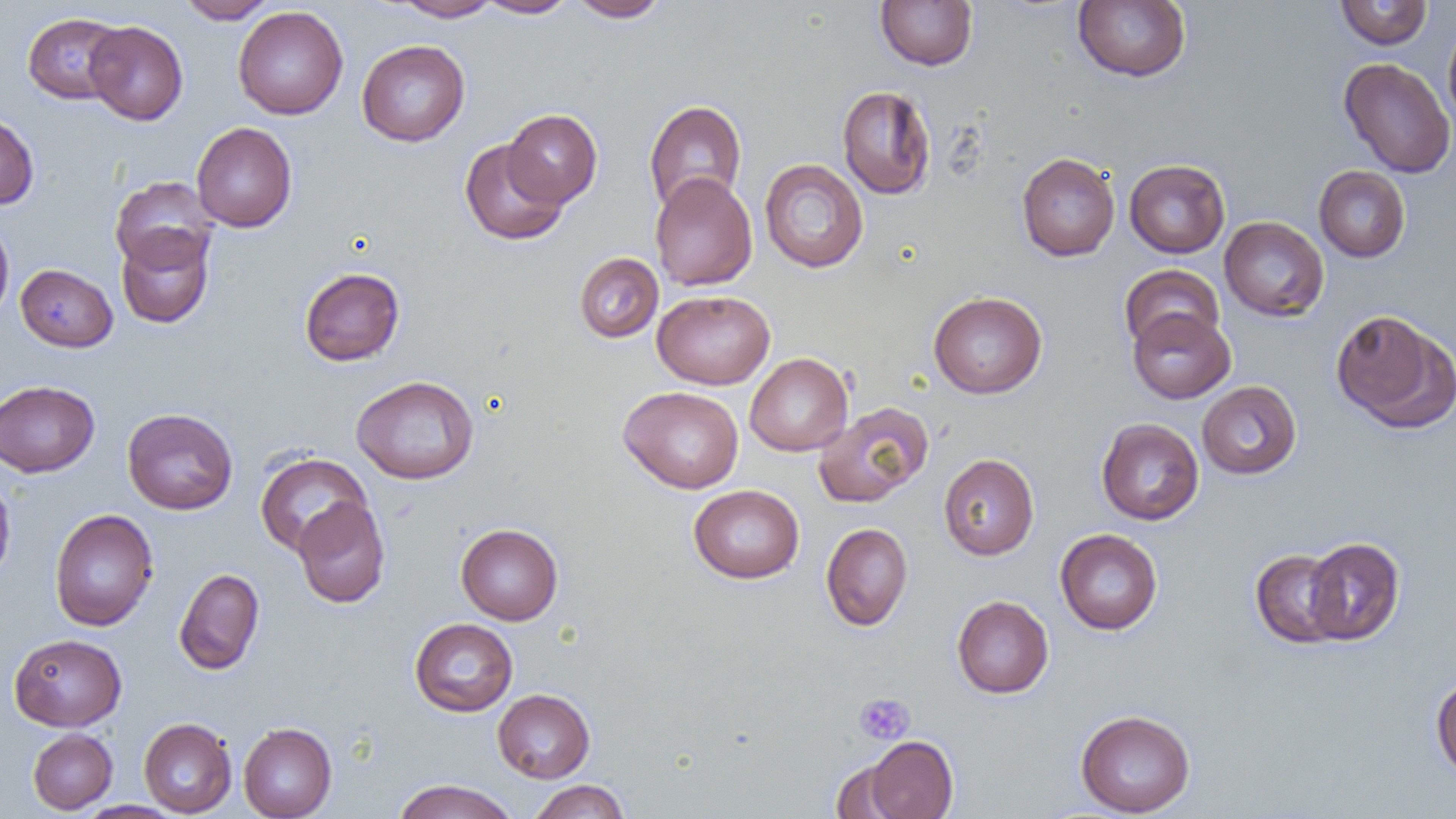
slide_level_diagnosis: no evidence of blood parasites
uninfected_red_blood_cell_locations: 'approximate bounding boxes as named x1/y1/x2/y2 corners in pixels: (x1=176, y1=0, x2=278, y2=24), (x1=390, y1=0, x2=500, y2=21), (x1=476, y1=0, x2=577, y2=18), (x1=567, y1=0, x2=671, y2=22), (x1=875, y1=0, x2=978, y2=70), (x1=1073, y1=0, x2=1191, y2=82), (x1=1334, y1=1, x2=1433, y2=50), (x1=233, y1=6, x2=348, y2=119), (x1=22, y1=12, x2=126, y2=104), (x1=84, y1=20, x2=188, y2=125), (x1=1443, y1=20, x2=1456, y2=132), (x1=356, y1=40, x2=470, y2=146), (x1=1338, y1=57, x2=1456, y2=179), (x1=837, y1=85, x2=936, y2=200), (x1=644, y1=100, x2=747, y2=213), (x1=503, y1=108, x2=602, y2=207), (x1=0, y1=111, x2=39, y2=210), (x1=191, y1=122, x2=297, y2=232), (x1=460, y1=139, x2=568, y2=245), (x1=1016, y1=152, x2=1120, y2=261), (x1=760, y1=158, x2=868, y2=273), (x1=1124, y1=159, x2=1230, y2=258), (x1=1313, y1=165, x2=1410, y2=262), (x1=650, y1=172, x2=757, y2=292), (x1=110, y1=176, x2=217, y2=273), (x1=0, y1=215, x2=14, y2=324), (x1=1219, y1=216, x2=1329, y2=321), (x1=116, y1=227, x2=215, y2=329), (x1=574, y1=252, x2=663, y2=343), (x1=15, y1=263, x2=118, y2=352), (x1=1119, y1=264, x2=1224, y2=351), (x1=299, y1=267, x2=404, y2=366), (x1=652, y1=290, x2=775, y2=389), (x1=928, y1=292, x2=1047, y2=398), (x1=1128, y1=307, x2=1235, y2=404), (x1=1330, y1=309, x2=1455, y2=432), (x1=744, y1=352, x2=853, y2=456), (x1=351, y1=375, x2=479, y2=484), (x1=0, y1=380, x2=100, y2=477), (x1=1197, y1=381, x2=1301, y2=479), (x1=619, y1=386, x2=744, y2=493), (x1=813, y1=401, x2=934, y2=508), (x1=122, y1=408, x2=238, y2=515), (x1=1096, y1=418, x2=1204, y2=525), (x1=255, y1=452, x2=371, y2=557), (x1=938, y1=453, x2=1039, y2=560), (x1=0, y1=474, x2=16, y2=586), (x1=688, y1=484, x2=804, y2=584), (x1=293, y1=498, x2=391, y2=608), (x1=49, y1=509, x2=159, y2=631), (x1=821, y1=522, x2=913, y2=631), (x1=456, y1=523, x2=563, y2=624), (x1=1055, y1=529, x2=1163, y2=635), (x1=1304, y1=537, x2=1405, y2=645), (x1=1250, y1=548, x2=1347, y2=648), (x1=174, y1=568, x2=265, y2=675), (x1=951, y1=595, x2=1054, y2=698), (x1=409, y1=618, x2=518, y2=716), (x1=9, y1=633, x2=126, y2=731), (x1=1431, y1=674, x2=1456, y2=780), (x1=493, y1=688, x2=595, y2=783), (x1=1075, y1=709, x2=1196, y2=817), (x1=139, y1=718, x2=237, y2=817), (x1=238, y1=722, x2=337, y2=819), (x1=27, y1=728, x2=117, y2=814), (x1=865, y1=735, x2=958, y2=819), (x1=829, y1=760, x2=909, y2=819), (x1=391, y1=779, x2=519, y2=819), (x1=528, y1=780, x2=631, y2=818), (x1=74, y1=801, x2=185, y2=819)'
platelet_locations: 'approximate bounding boxes as named x1/y1/x2/y2 corners in pixels: (x1=853, y1=693, x2=915, y2=745)'
image_size: 1456×819 pixels
magnification: 1000x
field_of_view: single
preparation: thin blood film
modality: optical microscopy